Report the malaria status of this cell.
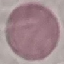
Uninfected.

Giemsa-stained preparation. Photographed with a smartphone camera at the microscope eyepiece. Thin blood film. Cell patch, automatically extracted from a larger field of view and resized to 64 × 64 pixels.